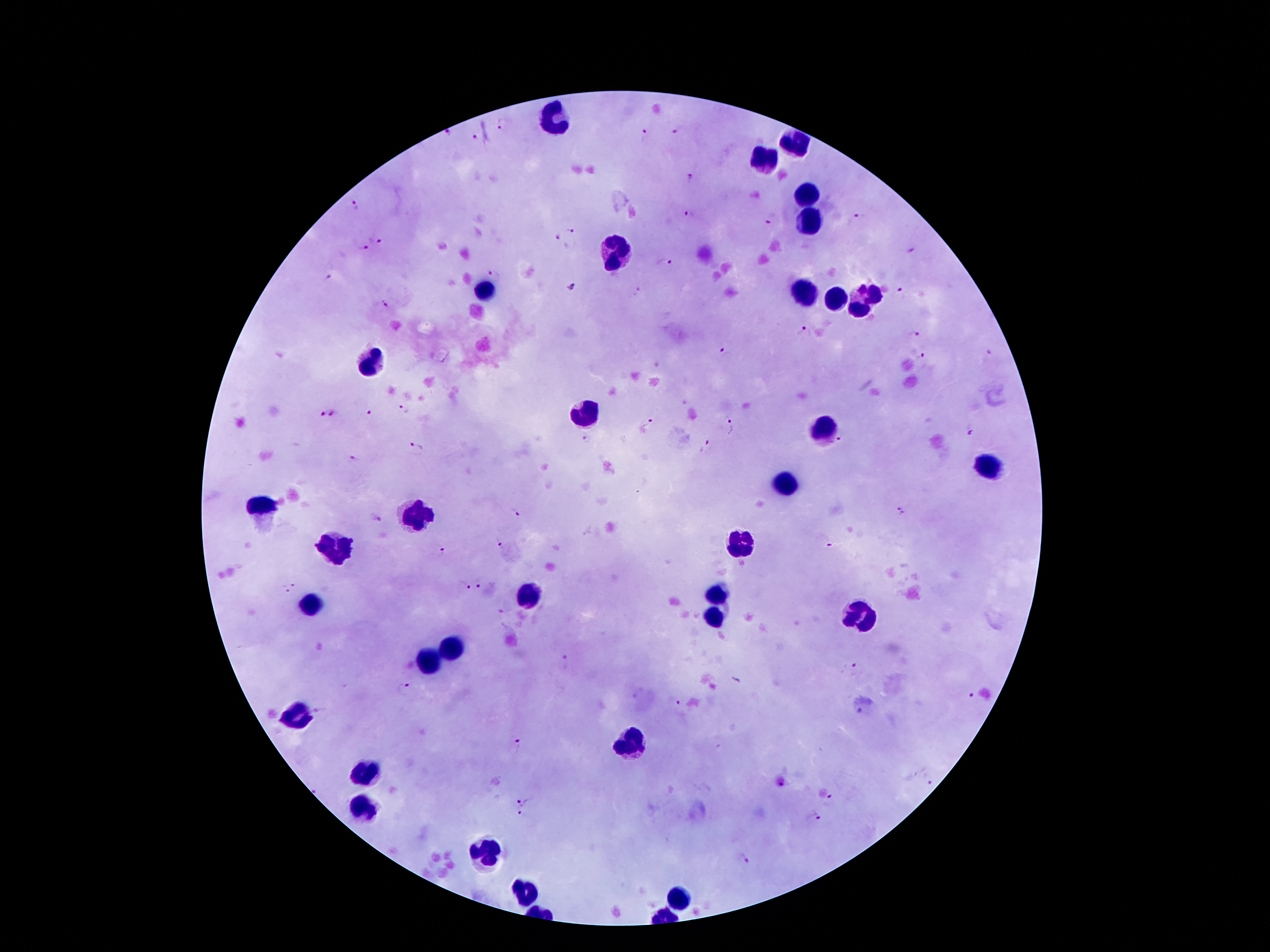
Approximate centers as (x, y) in pixels.
Summary:
  - Leukocyte locations: (554, 115), (799, 143), (765, 161), (808, 195), (810, 218), (617, 252), (484, 289), (802, 292), (836, 298), (865, 301), (370, 363), (584, 416), (826, 426), (986, 464), (783, 484), (259, 508), (418, 514), (336, 544), (738, 547), (717, 595), (527, 598), (313, 602), (860, 616), (717, 617), (454, 650), (427, 663), (298, 716), (631, 745), (366, 775), (363, 809), (481, 851), (527, 891), (677, 898)
  - Plasmodium parasite locations: (503, 125), (680, 129), (647, 134), (478, 137), (691, 181), (357, 206), (690, 217), (860, 219), (770, 220), (572, 232), (557, 238), (380, 239), (364, 250), (911, 251), (664, 263), (496, 274), (327, 278), (571, 288), (638, 290), (900, 292), (384, 306), (803, 331), (914, 335), (724, 353), (920, 357), (406, 409), (369, 412), (321, 414), (333, 414), (653, 420), (734, 425), (972, 430), (841, 438), (586, 440), (416, 446), (706, 448), (353, 459), (899, 511), (514, 513), (376, 516), (500, 543), (830, 547), (442, 551), (294, 585), (483, 585), (462, 586), (284, 590), (565, 660), (854, 667), (406, 688), (970, 693), (679, 705), (518, 746), (927, 782), (525, 799), (830, 801), (519, 813), (817, 820), (744, 861)
  - Magnification: 100x
  - Field of view: one from this slide
  - Patient malaria status: infected with Plasmodium falciparum
  - Stain: Giemsa
  - Preparation: thick blood smear
  - Capture: smartphone through the microscope eyepiece
  - Image size: 1270×952 pixels